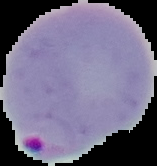 From a thin blood smear. The area outside the segmented cell region is set to black. Image is 157×166 pixels. Malaria status: parasitized.